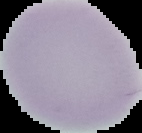 From a thin blood smear. Malaria status: uninfected. The area outside the segmented cell region is set to black. Image is 142×133 pixels.